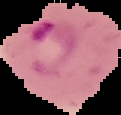 Cell region segmented out of the field of view; the surrounding area is masked to black. Result: Plasmodium parasites identified. Image is 121×115 pixels. From a thin blood smear.